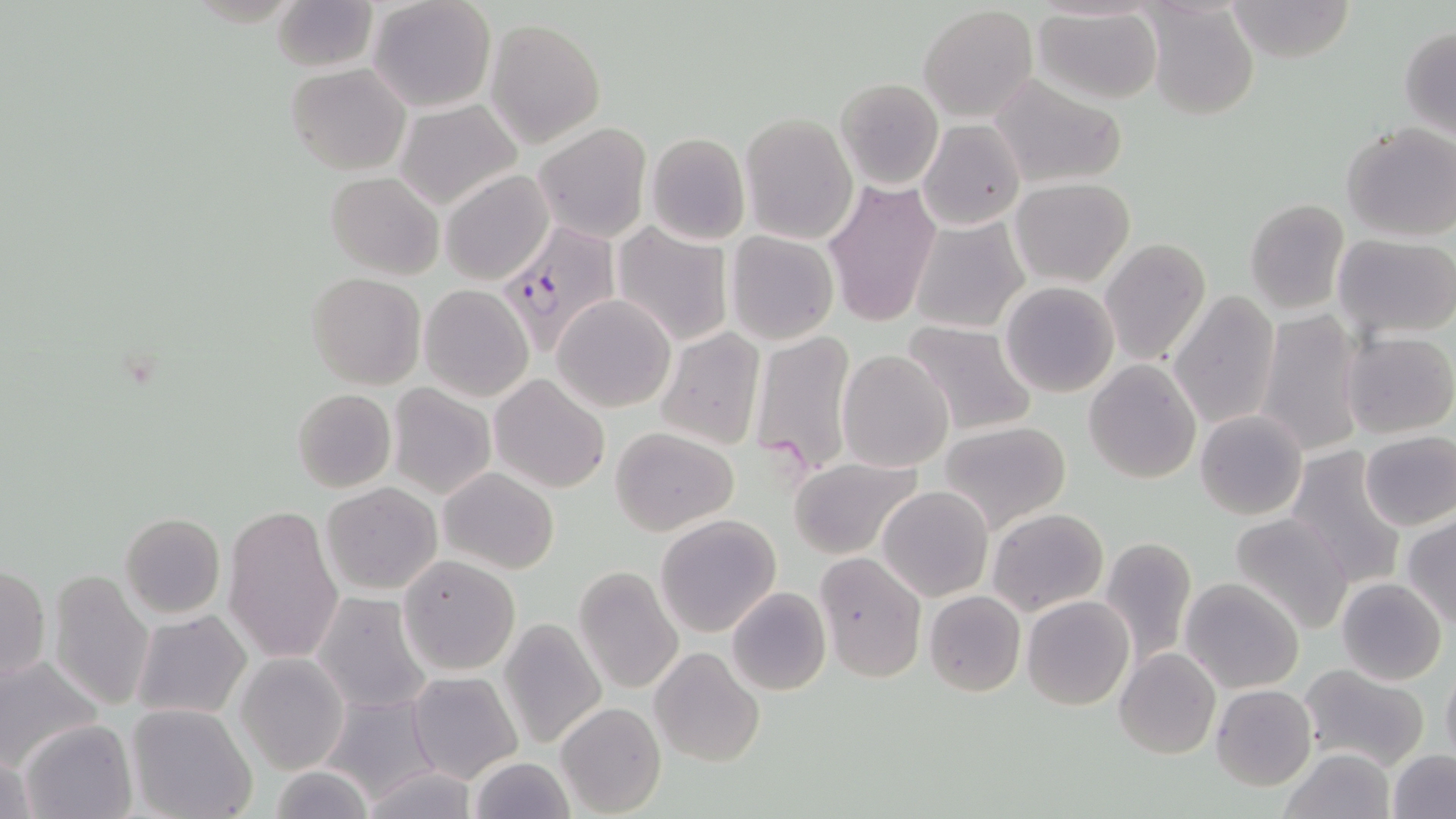

Approximate bounding boxes as named x1/y1/x2/y2 corners in pixels. Uninfected red blood cell locations: (x1=368, y1=0, x2=497, y2=114), (x1=1227, y1=0, x2=1356, y2=63), (x1=270, y1=1, x2=377, y2=73), (x1=1143, y1=3, x2=1261, y2=122), (x1=918, y1=4, x2=1037, y2=122), (x1=1032, y1=5, x2=1164, y2=105), (x1=485, y1=17, x2=607, y2=148), (x1=1399, y1=26, x2=1456, y2=137), (x1=285, y1=63, x2=411, y2=175), (x1=989, y1=74, x2=1129, y2=192), (x1=834, y1=77, x2=944, y2=190), (x1=393, y1=99, x2=523, y2=211), (x1=740, y1=112, x2=858, y2=245), (x1=918, y1=119, x2=1026, y2=231), (x1=533, y1=122, x2=652, y2=244), (x1=1340, y1=123, x2=1455, y2=241), (x1=645, y1=133, x2=750, y2=246), (x1=441, y1=170, x2=554, y2=287), (x1=325, y1=173, x2=442, y2=278), (x1=822, y1=177, x2=941, y2=329), (x1=1010, y1=177, x2=1134, y2=287), (x1=1245, y1=198, x2=1350, y2=316), (x1=909, y1=217, x2=1030, y2=334), (x1=612, y1=223, x2=734, y2=347), (x1=725, y1=231, x2=840, y2=346), (x1=1334, y1=232, x2=1456, y2=342), (x1=1100, y1=238, x2=1212, y2=369), (x1=307, y1=273, x2=426, y2=390), (x1=1001, y1=282, x2=1120, y2=398), (x1=419, y1=283, x2=534, y2=402), (x1=1169, y1=289, x2=1281, y2=431), (x1=553, y1=295, x2=675, y2=413), (x1=1254, y1=308, x2=1366, y2=459), (x1=902, y1=320, x2=1038, y2=436), (x1=655, y1=327, x2=766, y2=452), (x1=751, y1=328, x2=860, y2=477), (x1=1340, y1=330, x2=1455, y2=439), (x1=836, y1=348, x2=956, y2=472), (x1=1083, y1=358, x2=1202, y2=484), (x1=491, y1=373, x2=611, y2=494), (x1=388, y1=384, x2=495, y2=500), (x1=291, y1=388, x2=397, y2=494), (x1=1193, y1=409, x2=1308, y2=520), (x1=937, y1=421, x2=1071, y2=534), (x1=610, y1=426, x2=738, y2=535), (x1=1358, y1=429, x2=1456, y2=530), (x1=1286, y1=447, x2=1405, y2=589), (x1=789, y1=457, x2=923, y2=560), (x1=438, y1=468, x2=559, y2=574), (x1=322, y1=483, x2=442, y2=596), (x1=878, y1=485, x2=993, y2=601), (x1=225, y1=505, x2=344, y2=665), (x1=986, y1=508, x2=1108, y2=615), (x1=1229, y1=511, x2=1356, y2=634), (x1=119, y1=512, x2=225, y2=617), (x1=654, y1=515, x2=783, y2=638), (x1=1403, y1=515, x2=1456, y2=628), (x1=1098, y1=535, x2=1198, y2=666), (x1=815, y1=551, x2=925, y2=685), (x1=398, y1=554, x2=523, y2=677), (x1=1, y1=564, x2=50, y2=683), (x1=573, y1=566, x2=685, y2=697), (x1=48, y1=569, x2=155, y2=711), (x1=1180, y1=577, x2=1306, y2=694), (x1=1336, y1=578, x2=1447, y2=686), (x1=725, y1=586, x2=831, y2=697), (x1=924, y1=590, x2=1026, y2=697), (x1=312, y1=591, x2=434, y2=715), (x1=508, y1=593, x2=659, y2=725), (x1=1022, y1=596, x2=1134, y2=710), (x1=132, y1=611, x2=253, y2=721), (x1=499, y1=618, x2=606, y2=753), (x1=648, y1=646, x2=765, y2=767), (x1=1114, y1=648, x2=1221, y2=760), (x1=0, y1=654, x2=105, y2=773), (x1=235, y1=654, x2=349, y2=774), (x1=1299, y1=665, x2=1430, y2=771), (x1=1441, y1=666, x2=1456, y2=767), (x1=406, y1=671, x2=522, y2=784), (x1=1210, y1=683, x2=1316, y2=791), (x1=322, y1=693, x2=441, y2=804), (x1=126, y1=702, x2=257, y2=819), (x1=556, y1=702, x2=666, y2=817), (x1=17, y1=718, x2=137, y2=819), (x1=1, y1=746, x2=36, y2=819), (x1=1281, y1=747, x2=1396, y2=818), (x1=1386, y1=748, x2=1456, y2=819), (x1=467, y1=756, x2=574, y2=819), (x1=357, y1=765, x2=481, y2=819), (x1=266, y1=766, x2=374, y2=817). Plasmodium falciparum-infected red blood cell locations: (x1=496, y1=220, x2=622, y2=356). Slide-level diagnosis: Plasmodium falciparum. Light microscopy. Captured at 1000x magnification. One field of a larger specimen. May-Grünwald-Giemsa stain. Thin blood film. Image is 1456×819 pixels.